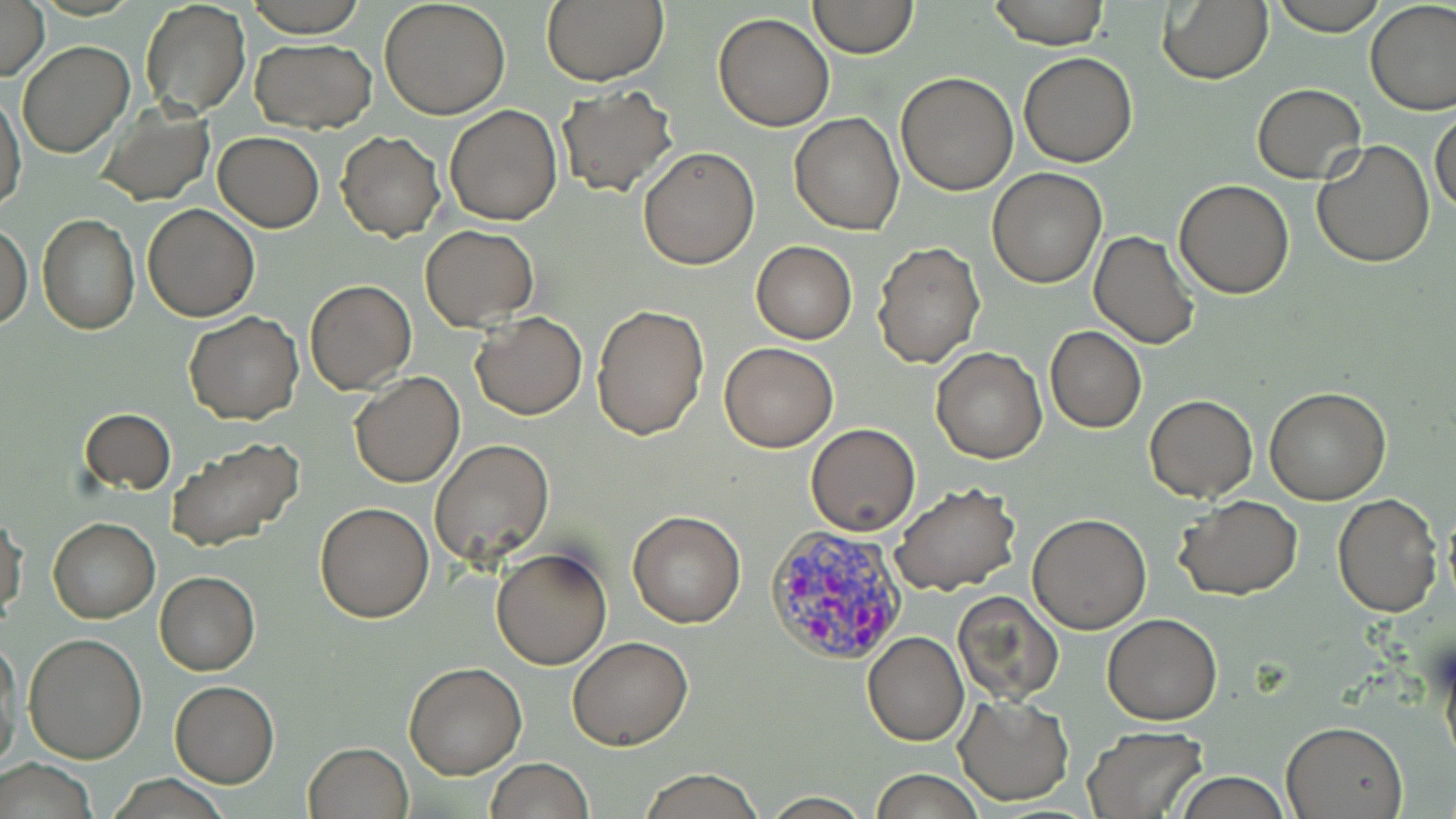
Summary:
  - Coordinate format: approximate bounding boxes as [x1, y1, x2, y2] in pixels
  - Uninfected red blood cell locations: [0, 0, 49, 82], [138, 0, 252, 120], [244, 0, 368, 36], [380, 0, 511, 118], [807, 0, 918, 58], [988, 0, 1110, 48], [1275, 0, 1386, 35], [1365, 0, 1456, 115], [540, 1, 670, 86], [1159, 2, 1274, 84], [713, 12, 835, 131], [250, 38, 376, 132], [17, 40, 135, 157], [1018, 52, 1139, 167], [895, 71, 1018, 193], [1250, 83, 1368, 183], [555, 85, 678, 198], [1, 86, 25, 216], [94, 104, 215, 205], [444, 104, 563, 224], [1431, 107, 1456, 218], [789, 112, 904, 234], [336, 130, 446, 241], [214, 131, 324, 232], [1311, 140, 1437, 267], [638, 146, 759, 268], [987, 167, 1107, 288], [1173, 180, 1294, 298], [142, 204, 259, 322], [37, 215, 141, 335], [0, 222, 31, 329], [420, 223, 539, 330], [1088, 230, 1199, 349], [751, 241, 857, 343], [874, 241, 984, 367], [303, 279, 416, 395], [591, 302, 709, 439], [185, 311, 304, 425], [469, 312, 588, 420], [1045, 326, 1147, 432], [719, 342, 837, 452], [931, 347, 1048, 463], [350, 372, 464, 488], [1265, 386, 1390, 504], [1145, 394, 1258, 501], [79, 408, 176, 494], [805, 422, 920, 536], [166, 437, 305, 553], [430, 439, 555, 565], [891, 485, 1021, 596], [1332, 493, 1443, 617], [1176, 495, 1302, 601], [315, 501, 435, 622], [627, 509, 746, 628], [1, 510, 26, 623], [1027, 513, 1152, 634], [48, 517, 161, 622], [492, 546, 612, 669], [154, 571, 260, 675], [952, 589, 1067, 705], [1102, 613, 1223, 724], [862, 631, 969, 745], [22, 633, 148, 763], [567, 636, 693, 750], [1441, 640, 1456, 776], [0, 641, 20, 777], [404, 662, 527, 778], [168, 680, 280, 788], [953, 695, 1074, 804], [1279, 721, 1407, 818], [1082, 727, 1209, 817], [305, 742, 413, 819], [486, 757, 595, 818], [1, 760, 98, 818], [637, 767, 767, 819], [869, 768, 983, 819], [1174, 772, 1293, 818], [106, 775, 233, 817], [761, 794, 875, 818]
  - Plasmodium vivax-infected red blood cell locations: [767, 525, 916, 670]
  - Slide-level diagnosis: Plasmodium vivax
  - Image size: 1456×819 pixels
  - Field of view: single
  - Modality: optical microscopy
  - Magnification: 1000x
  - Stain: May-Grünwald-Giemsa
  - Preparation: thin blood smear